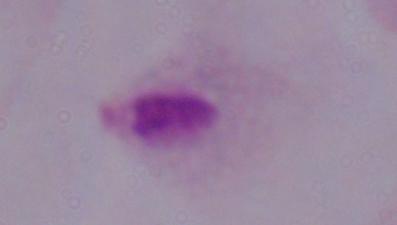
1000x magnification. Micrograph. A trichomonad is shown.